Identify the parasite.
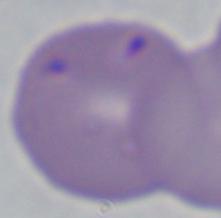
Babesia.

{
  "modality": "micrograph",
  "magnification": "1000x"
}